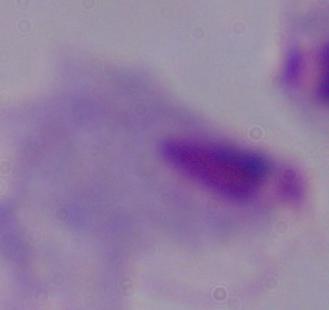
Captured at 1000x magnification. A trichomonad is seen. Micrograph.